Point out each Plasmodium parasite.
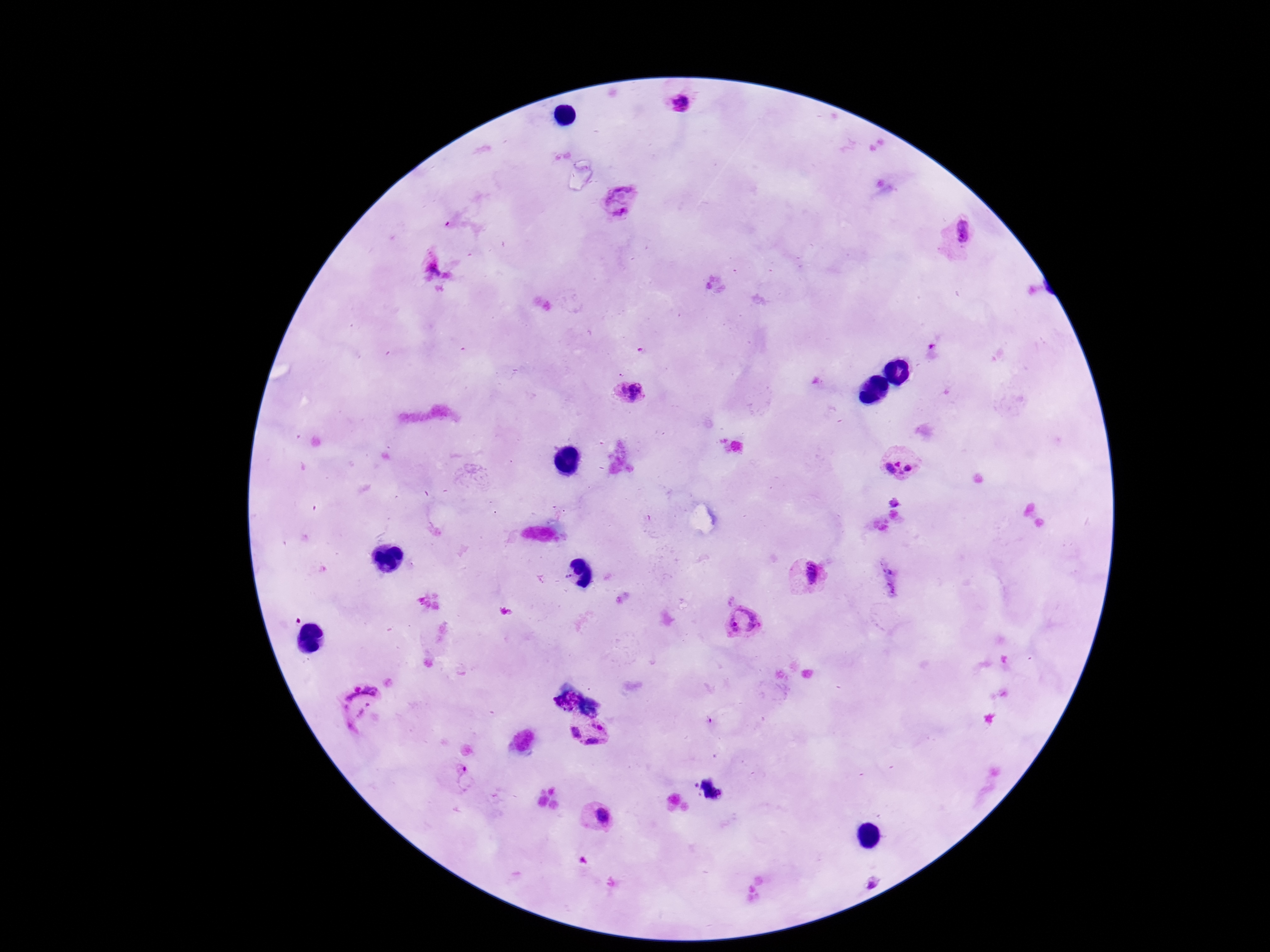

Approximate centers as [x, y] in pixels.
Plasmodium parasites: [679, 103], [620, 202], [957, 237], [433, 264], [630, 394], [902, 463], [809, 574], [743, 621], [362, 707], [589, 732], [458, 779], [599, 817], [871, 884].

Summary:
  - Field of view: single
  - Stain: Giemsa
  - Preparation: thick blood film
  - Magnification: 100x
  - Capture: smartphone camera through the microscope eyepiece
  - Patient malaria status: positive
  - Image size: 1270×952 pixels